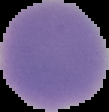

preparation: thin blood film
image_type: cell region segmented out of the field of view; surrounding area masked to black
result: negative for malaria parasites
image_size: 109×112 pixels